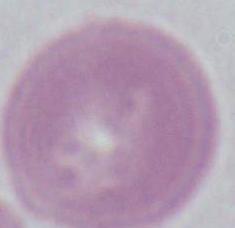

{
  "modality": "photomicrograph",
  "magnification": "1000x",
  "identification": "red blood cell"
}